Identify the blood parasite species.
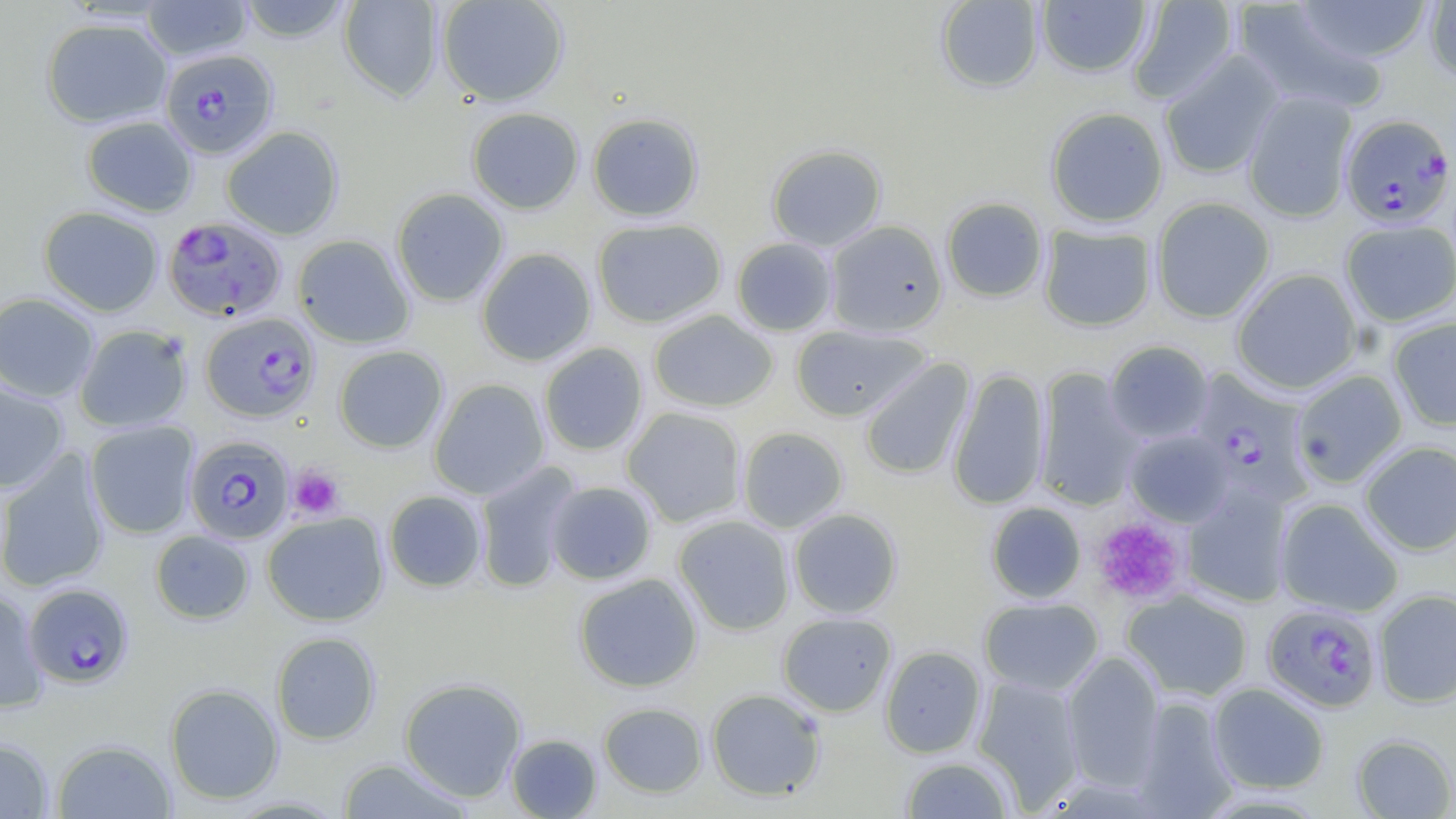

Plasmodium falciparum.

Approximate bounding boxes as (x1,y1)-(x2,y2) corner pairs in pixels. Uninfected red blood cell locations: (140,0)-(254,61), (236,0)-(355,42), (338,0)-(443,101), (436,0)-(570,106), (934,0)-(1044,94), (1035,0)-(1153,78), (1127,0)-(1240,105), (1292,0)-(1434,64), (1424,1)-(1456,85), (1232,2)-(1389,115), (41,18)-(172,128), (1158,51)-(1285,180), (1243,90)-(1358,223), (1044,106)-(1169,228), (466,107)-(584,214), (587,113)-(704,222), (81,115)-(198,217), (221,126)-(344,240), (766,144)-(887,252), (391,188)-(509,307), (941,197)-(1048,303), (1151,197)-(1275,323), (38,206)-(164,317), (592,218)-(727,328), (1340,219)-(1456,327), (825,220)-(948,338), (1038,224)-(1157,332), (293,234)-(415,348), (731,237)-(837,336), (476,247)-(597,366), (1231,268)-(1362,395), (0,292)-(100,403), (648,310)-(778,413), (1388,316)-(1456,432), (75,324)-(193,433), (790,325)-(931,421), (1104,340)-(1214,444), (538,342)-(649,456), (334,345)-(449,452), (859,358)-(975,480), (947,368)-(1050,510), (1034,368)-(1144,511), (1290,370)-(1408,489), (428,378)-(551,500), (0,382)-(69,494), (621,407)-(747,527), (85,420)-(199,539), (736,427)-(849,533), (1125,429)-(1233,527), (1359,441)-(1456,555), (0,448)-(110,593), (474,460)-(581,594), (545,481)-(657,585), (1182,483)-(1294,608), (384,490)-(486,592), (1275,498)-(1404,617), (986,502)-(1086,604), (788,508)-(903,618), (262,511)-(389,626), (673,515)-(796,636), (150,530)-(254,624), (573,573)-(703,692), (0,590)-(48,713), (1122,590)-(1254,702), (1373,590)-(1456,708), (979,597)-(1104,696), (777,612)-(897,717), (271,632)-(381,745), (880,645)-(987,758), (1062,651)-(1164,789), (972,676)-(1085,810), (398,677)-(527,801), (164,683)-(284,804), (1208,683)-(1329,794), (706,688)-(827,801), (1132,697)-(1239,818), (598,702)-(707,797), (505,733)-(602,818), (1351,734)-(1456,818), (0,738)-(54,818), (52,739)-(176,818), (900,756)-(1015,818), (335,758)-(475,818). Plasmodium falciparum-infected red blood cell locations: (161,49)-(278,159), (1340,115)-(1455,228), (162,215)-(286,322), (200,312)-(320,422), (1192,371)-(1315,508), (185,435)-(295,544), (24,583)-(134,688), (1262,603)-(1382,712). Platelet locations: (289,464)-(345,520), (1092,517)-(1187,605). Thin blood smear. May-Grünwald-Giemsa-stained preparation. Image is 1456×819 pixels. One field of a larger specimen. Captured at 1000x magnification. Light microscopy.